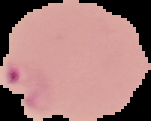 Image is 151×121 pixels. Malaria status: parasitized. The area outside the segmented cell region is set to black. From a thin blood smear.